State which parasite is depicted.
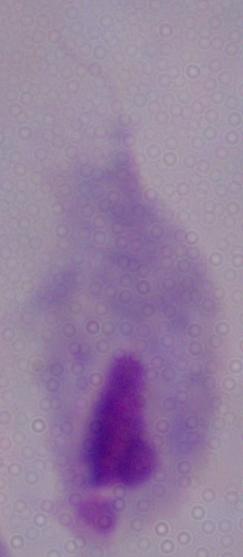

This is a trichomonad.

modality = photomicrograph
magnification = 1000x